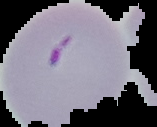

image size = 157×127 pixels
preparation = thin blood film
result = malaria parasites detected
image type = cell region segmented out of the field of view; surrounding area masked to black